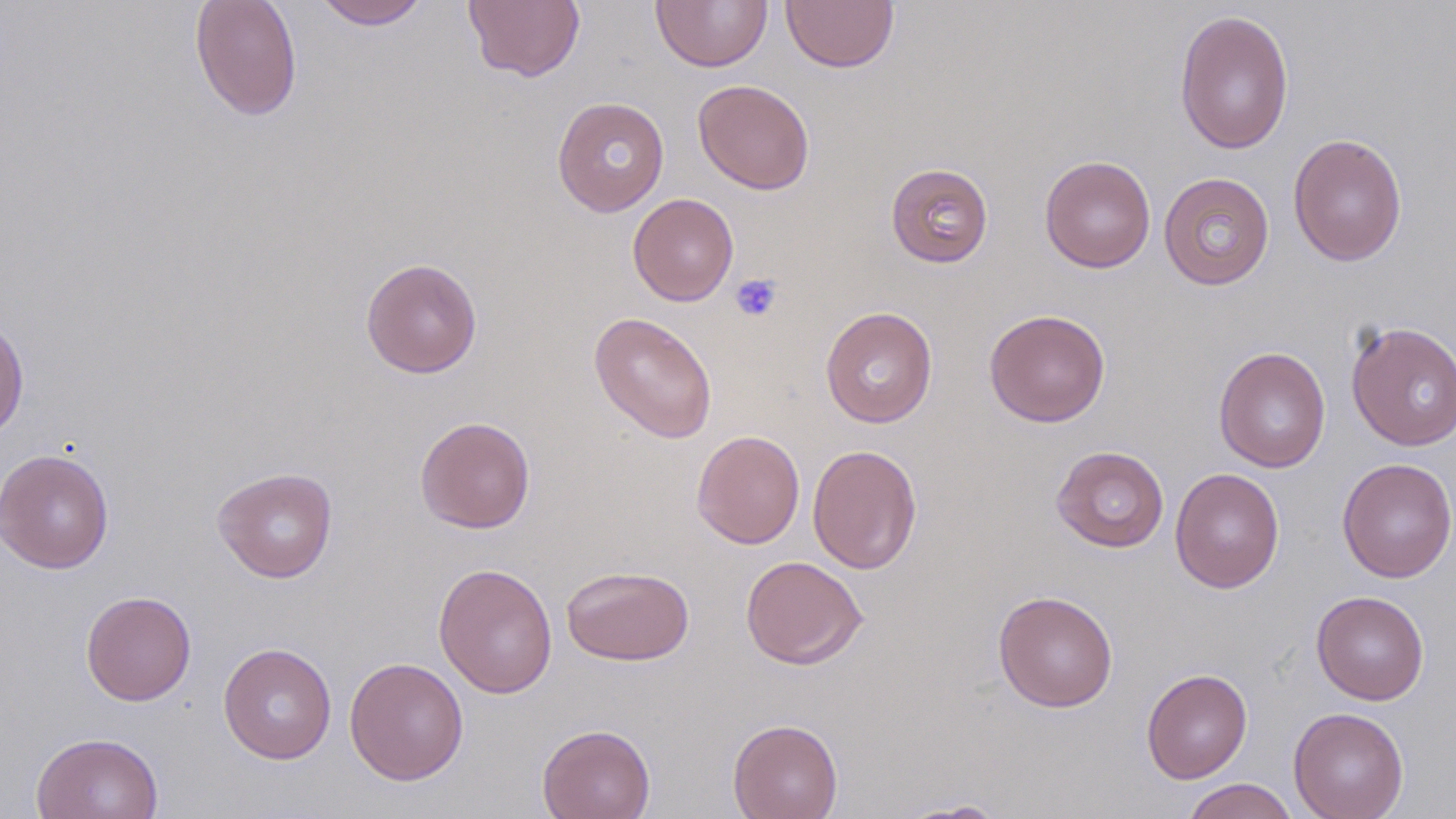

Approximate bounding boxes as (x1, y1, x2, y2) in pixels. Uninfected red blood cell locations: (313, 0, 430, 29), (462, 0, 585, 83), (650, 0, 773, 72), (780, 0, 900, 73), (189, 1, 303, 122), (1174, 9, 1294, 155), (692, 79, 815, 194), (552, 96, 670, 217), (1287, 133, 1408, 266), (1039, 155, 1156, 273), (886, 163, 994, 268), (1158, 172, 1274, 290), (628, 193, 738, 306), (360, 257, 483, 378), (820, 306, 938, 428), (984, 308, 1110, 427), (588, 311, 718, 444), (0, 313, 29, 442), (1345, 321, 1456, 451), (1213, 346, 1332, 473), (415, 416, 535, 533), (691, 430, 805, 549), (807, 444, 922, 575), (1051, 445, 1169, 552), (0, 447, 115, 574), (1336, 457, 1456, 582), (212, 466, 338, 583), (1170, 467, 1285, 594), (740, 555, 869, 670), (433, 562, 558, 699), (561, 565, 695, 666), (81, 590, 196, 705), (993, 590, 1118, 712), (1311, 590, 1429, 705), (218, 642, 337, 764), (344, 657, 469, 785), (1141, 668, 1252, 784), (1288, 707, 1410, 819), (728, 718, 843, 819), (537, 724, 656, 819), (31, 731, 164, 819), (1181, 778, 1299, 819), (895, 798, 1012, 818). Platelet locations: (730, 273, 782, 322). Slide-level diagnosis: negative for blood parasites. May-Grünwald-Giemsa stain. Light microscopy. Single field of view. Thin blood smear. 1000x magnification. Image is 1456×819 pixels.